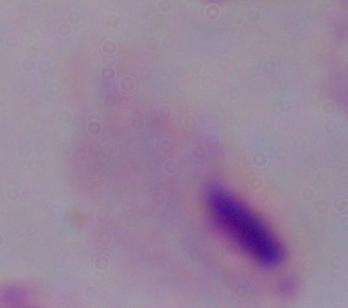

modality: photomicrograph
magnification: 1000x
identification: trichomonad